Describe the morphology of the red blood cells.
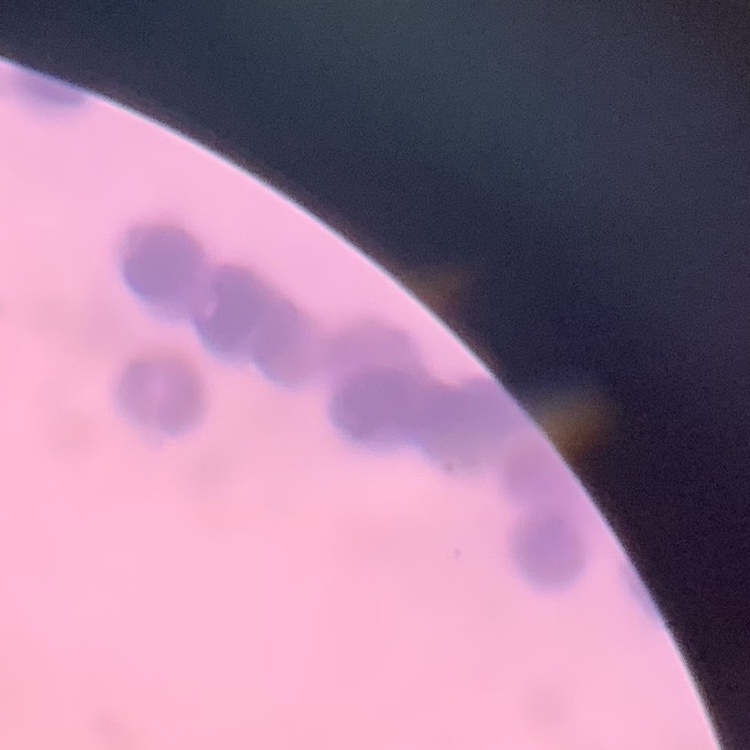

Rouleaux formation.

image type = square crop of a larger photomicrograph
stain = Field's or Giemsa
preparation = thin peripheral smear